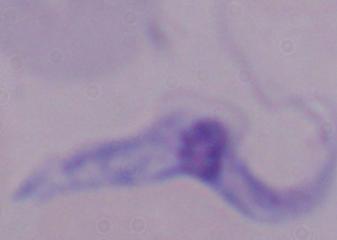
Summary:
  - Magnification: 1000x
  - Modality: micrograph
  - Identification: trypanosome